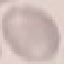
Summary:
  - Result: no malaria parasites detected
  - Capture: smartphone through the microscope eyepiece
  - Stain: Giemsa
  - Image type: cell patch, automatically extracted from a larger field of view and resized to 64 × 64 pixels
  - Preparation: thin smear